Evaluate for malaria.
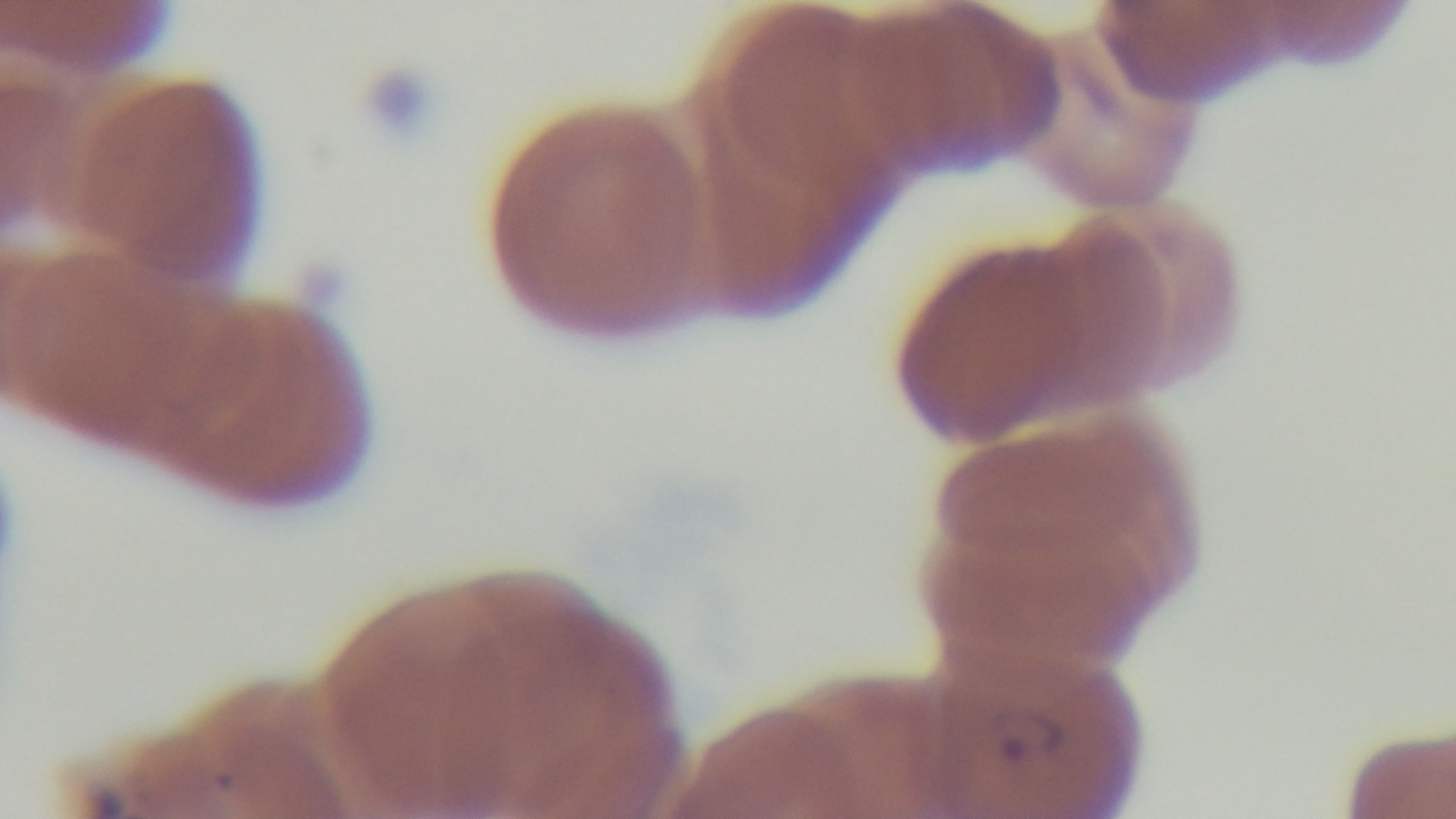
Positive.

capture = mounted 4K digital camera
preparation = thin blood film
objective = 100x oil immersion
modality = light microscopy
field of view = single
stain = Giemsa